Locate and identify every blood parasite.
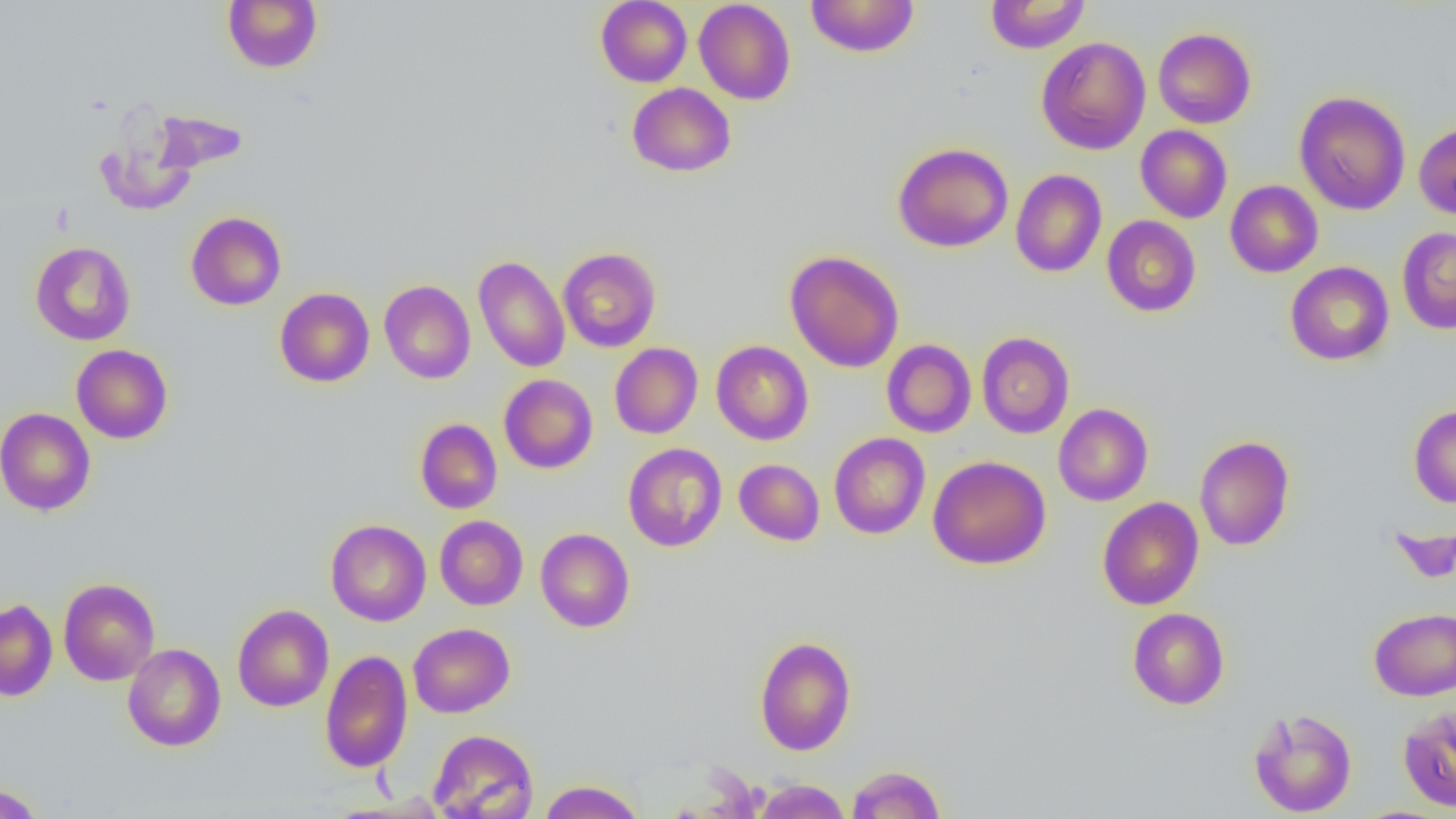

No blood parasites seen.

slide-level diagnosis = no evidence of blood parasites
field of view = single
modality = optical microscopy
preparation = thin blood smear
uninfected red blood cell locations = approximate bounding boxes as named x1/y1/x2/y2 corners in pixels: (x1=222, y1=0, x2=323, y2=73), (x1=595, y1=0, x2=692, y2=87), (x1=805, y1=0, x2=919, y2=57), (x1=985, y1=0, x2=1090, y2=53), (x1=694, y1=1, x2=796, y2=105), (x1=1153, y1=27, x2=1256, y2=128), (x1=1036, y1=36, x2=1150, y2=155), (x1=627, y1=83, x2=736, y2=177), (x1=1294, y1=91, x2=1410, y2=215), (x1=150, y1=108, x2=248, y2=175), (x1=95, y1=116, x2=200, y2=217), (x1=1414, y1=122, x2=1456, y2=220), (x1=1135, y1=125, x2=1232, y2=223), (x1=892, y1=142, x2=1013, y2=253), (x1=1010, y1=169, x2=1107, y2=277), (x1=1225, y1=180, x2=1323, y2=277), (x1=186, y1=212, x2=286, y2=310), (x1=1102, y1=215, x2=1201, y2=317), (x1=1397, y1=227, x2=1456, y2=333), (x1=30, y1=241, x2=136, y2=345), (x1=557, y1=247, x2=661, y2=352), (x1=785, y1=250, x2=904, y2=372), (x1=473, y1=255, x2=570, y2=373), (x1=1285, y1=261, x2=1394, y2=365), (x1=379, y1=279, x2=475, y2=383), (x1=275, y1=287, x2=374, y2=387), (x1=976, y1=331, x2=1074, y2=438), (x1=882, y1=339, x2=976, y2=438), (x1=712, y1=340, x2=813, y2=445), (x1=610, y1=343, x2=703, y2=439), (x1=71, y1=344, x2=173, y2=444), (x1=499, y1=374, x2=597, y2=473), (x1=1053, y1=403, x2=1153, y2=506), (x1=1408, y1=404, x2=1456, y2=507), (x1=0, y1=407, x2=96, y2=516), (x1=415, y1=418, x2=502, y2=514), (x1=829, y1=432, x2=930, y2=539), (x1=1194, y1=435, x2=1295, y2=551), (x1=623, y1=443, x2=727, y2=552), (x1=928, y1=455, x2=1051, y2=570), (x1=734, y1=459, x2=824, y2=545), (x1=1097, y1=497, x2=1204, y2=610), (x1=434, y1=515, x2=528, y2=610), (x1=325, y1=519, x2=431, y2=626), (x1=535, y1=528, x2=635, y2=632), (x1=58, y1=578, x2=160, y2=685), (x1=0, y1=599, x2=58, y2=701), (x1=232, y1=604, x2=334, y2=711), (x1=1127, y1=607, x2=1230, y2=709), (x1=1369, y1=607, x2=1456, y2=700), (x1=408, y1=623, x2=515, y2=718), (x1=754, y1=635, x2=856, y2=755), (x1=123, y1=643, x2=226, y2=751), (x1=319, y1=649, x2=413, y2=773), (x1=1398, y1=705, x2=1456, y2=811), (x1=1247, y1=707, x2=1357, y2=817), (x1=427, y1=729, x2=539, y2=819), (x1=846, y1=764, x2=946, y2=818), (x1=538, y1=779, x2=645, y2=819), (x1=752, y1=779, x2=851, y2=819), (x1=0, y1=783, x2=45, y2=819)
image size = 1456×819 pixels
magnification = 1000x